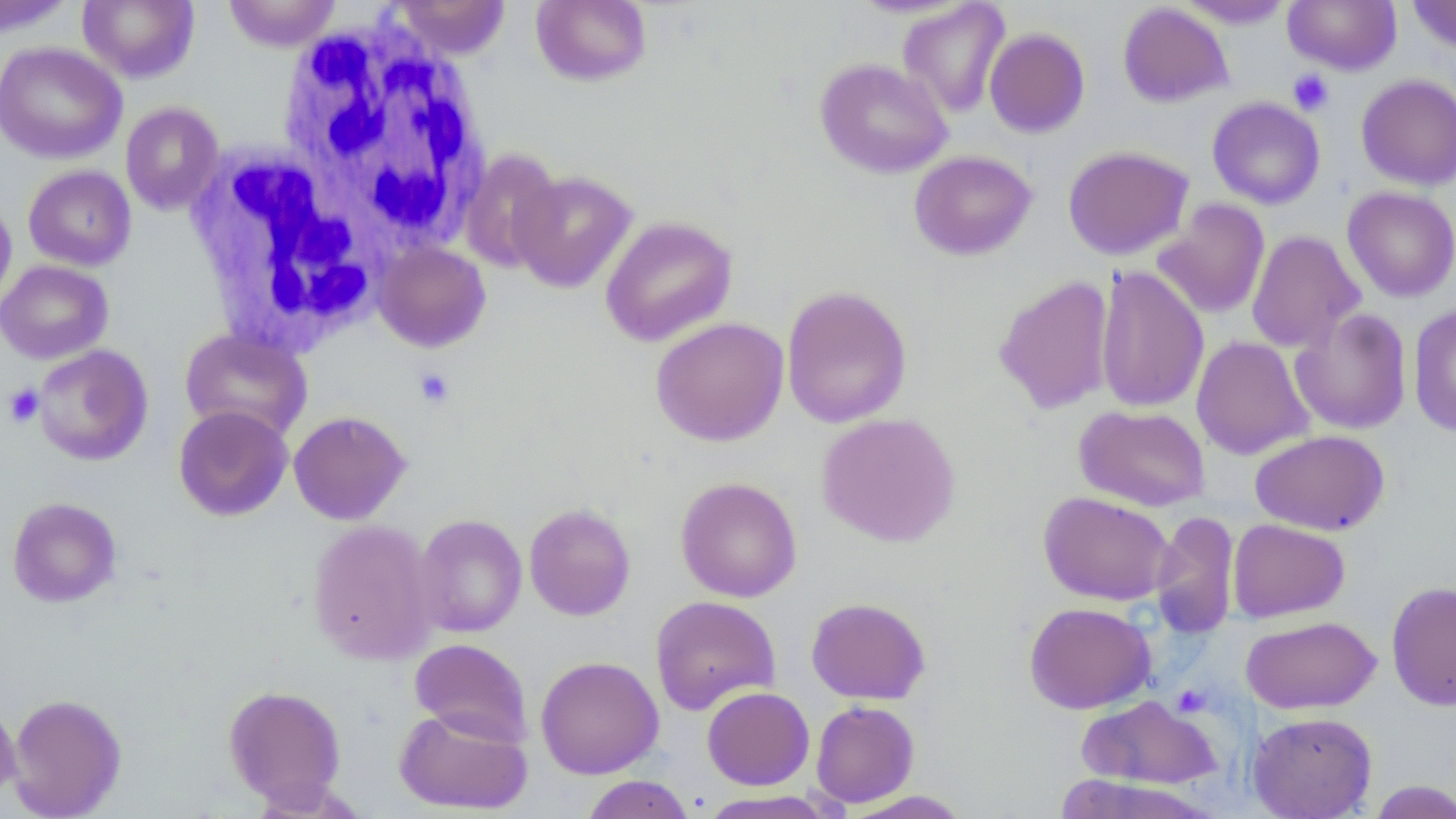

Approximate bounding boxes as (x1,y1)-(x2,y2) corner pairs in pixels. White blood cell locations: (276,17)-(495,255), (185,143)-(387,351). Platelet locations: (1288,69)-(1333,114), (414,368)-(455,408), (3,383)-(44,428), (1172,684)-(1210,717). Uninfected red blood cell locations: (0,0)-(77,38), (77,0)-(200,83), (222,0)-(342,52), (390,0)-(512,60), (1176,0)-(1294,29), (1408,0)-(1456,55), (531,1)-(651,87), (897,1)-(1010,118), (1283,1)-(1401,74), (1117,2)-(1233,107), (984,27)-(1090,138), (0,42)-(127,164), (815,57)-(953,178), (1356,74)-(1456,190), (1207,96)-(1325,210), (120,102)-(225,215), (1062,145)-(1193,260), (459,148)-(564,274), (909,150)-(1036,261), (23,165)-(136,271), (509,169)-(637,293), (1342,186)-(1456,302), (0,190)-(17,311), (1152,199)-(1271,319), (600,215)-(738,347), (1246,230)-(1364,353), (373,241)-(492,352), (0,260)-(113,364), (1094,265)-(1209,414), (994,274)-(1115,415), (781,285)-(912,428), (1408,301)-(1456,437), (1290,307)-(1412,435), (650,317)-(789,446), (179,327)-(312,442), (1191,335)-(1313,460), (32,344)-(154,466), (1074,404)-(1211,511), (173,405)-(293,521), (288,410)-(411,525), (817,412)-(960,547), (1251,430)-(1389,536), (676,476)-(802,602), (1038,491)-(1174,606), (7,497)-(122,608), (524,503)-(636,620), (1149,511)-(1239,638), (413,514)-(527,637), (307,519)-(438,666), (1228,519)-(1349,622), (1386,580)-(1456,711), (650,595)-(780,715), (805,597)-(931,705), (1023,602)-(1155,714), (1241,615)-(1380,714), (409,638)-(532,745), (535,656)-(663,779), (223,685)-(347,808), (702,686)-(815,790), (7,693)-(127,818), (1076,695)-(1220,790), (811,700)-(920,808), (0,701)-(20,806), (394,706)-(532,815), (1248,712)-(1377,818), (1059,772)-(1217,818), (579,775)-(696,819), (1366,780)-(1456,818), (842,790)-(971,819), (696,791)-(840,819). Slide-level diagnosis: no evidence of blood parasites. May-Grünwald-Giemsa stain. Captured at 1000x magnification. Optical microscopy. Image is 1456×819 pixels. Thin blood film. One field of a larger specimen.